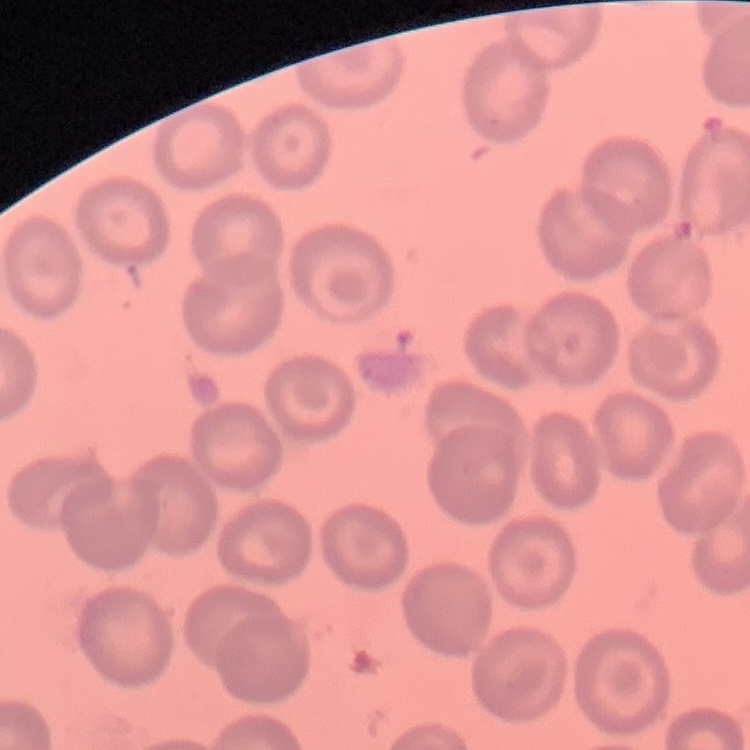

Summary:
  - Red blood cell morphology: no rouleaux formation
  - Image type: one tile cut from a larger photomicrograph
  - Preparation: thin blood film
  - Stain: Field's or Giemsa